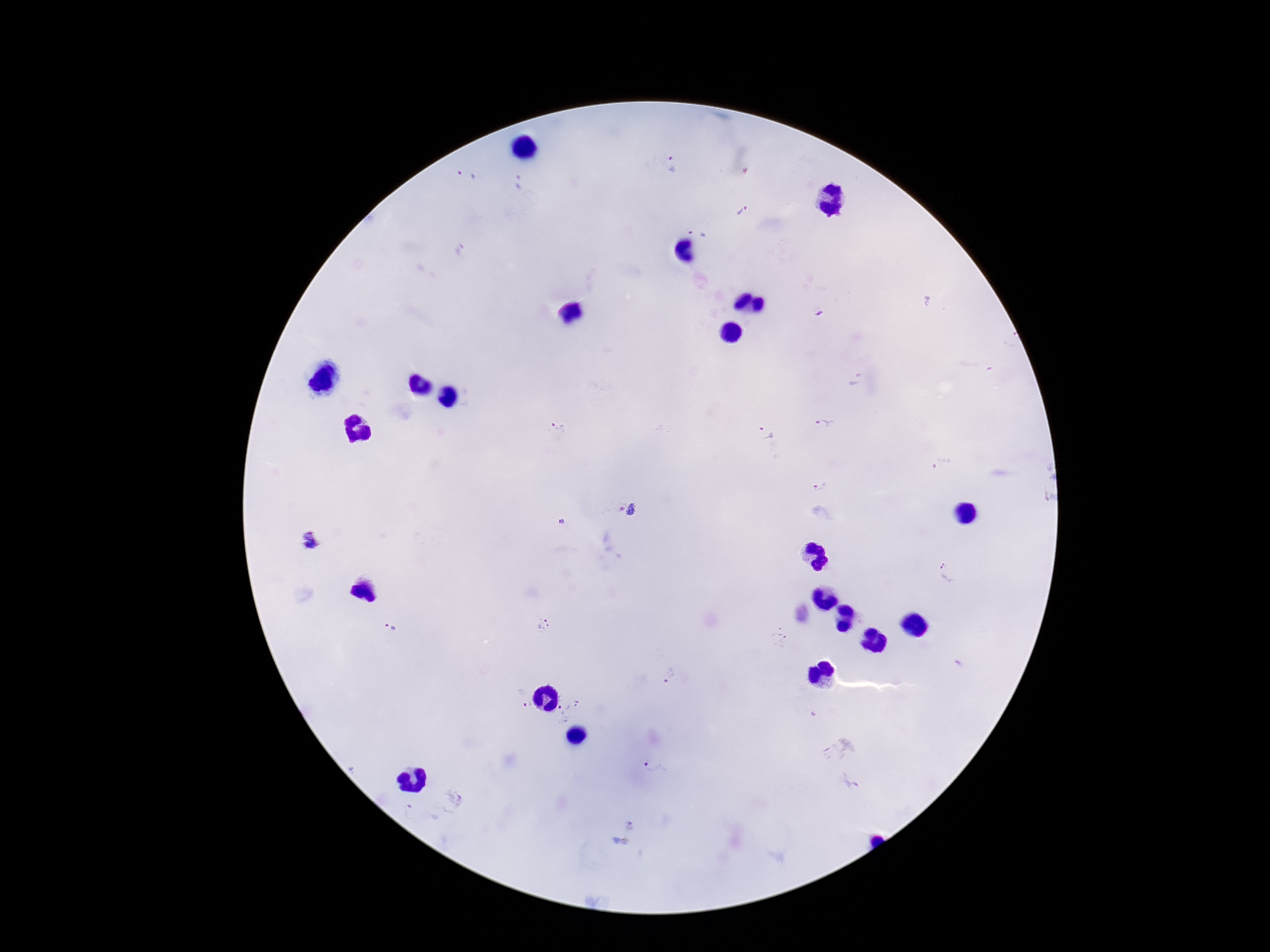

Approximate centers as {x, y} in pixels. Plasmodium parasite locations: {671, 165}, {467, 174}, {519, 183}, {742, 210}, {700, 231}, {819, 313}, {560, 428}, {824, 428}, {767, 436}, {943, 467}, {1048, 486}, {819, 487}, {618, 508}, {634, 511}, {563, 523}, {310, 538}, {948, 571}, {543, 625}, {391, 628}, {779, 637}, {669, 676}, {529, 704}, {573, 705}, {561, 717}, {838, 748}, {656, 767}, {449, 801}, {412, 813}, {622, 831}. Patient malaria status: positive. One field from this slide. Smartphone photograph taken through the microscope eyepiece. Giemsa stain. 100x magnification. Thick blood smear. Image is 1270×952 pixels.